Give the extent of all Plasmodium ovale-infected red blood cells.
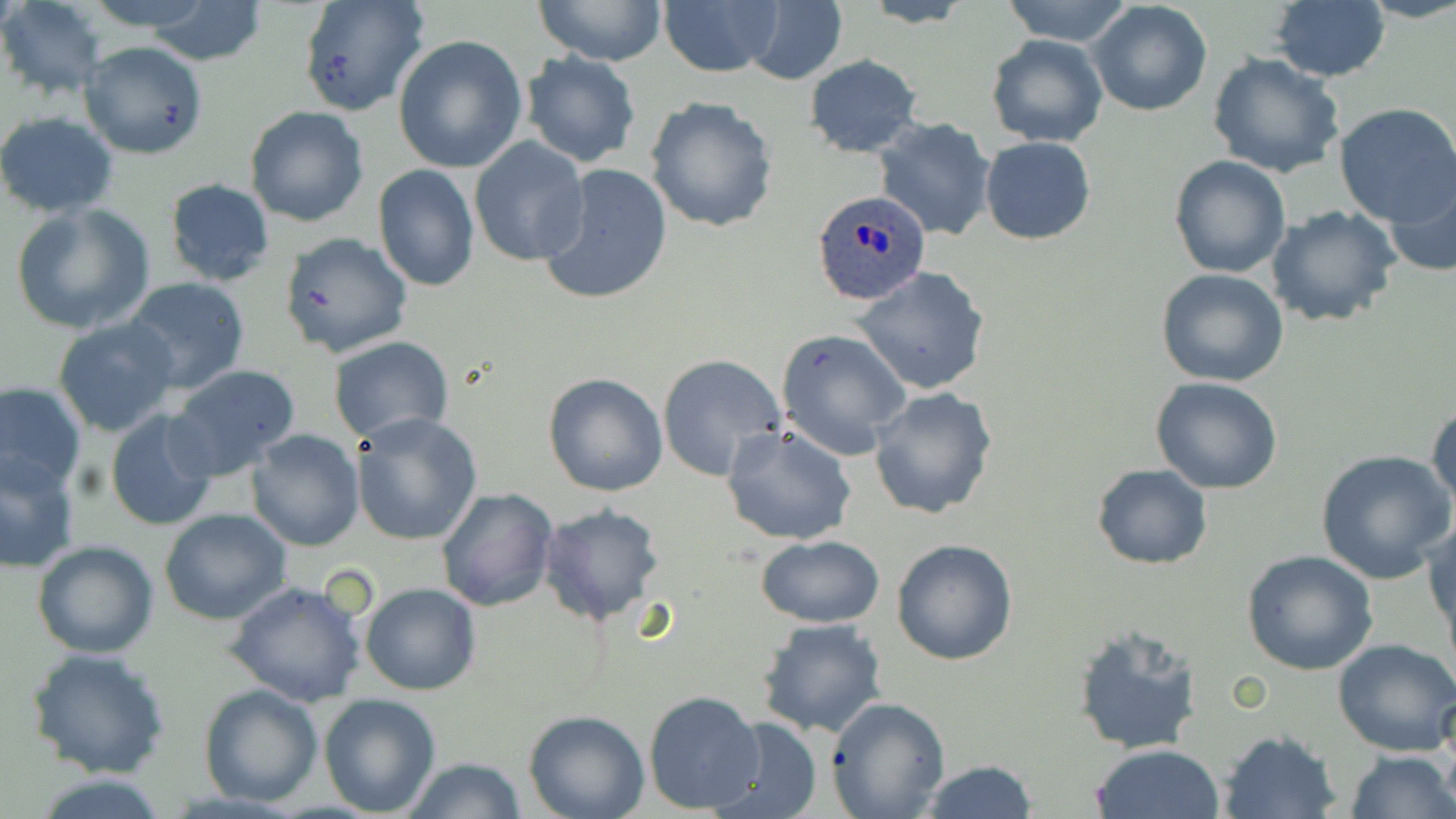

Approximate bounding boxes as (x1, y1, x2, y2) in pixels.
Plasmodium ovale-infected red blood cells: (810, 189, 930, 306).

Uninfected red blood cell locations: (1, 0, 108, 98), (80, 0, 223, 32), (297, 0, 429, 117), (537, 0, 666, 67), (739, 0, 849, 85), (998, 0, 1136, 46), (857, 1, 980, 28), (1268, 1, 1391, 83), (137, 2, 267, 65), (658, 2, 780, 78), (1088, 2, 1213, 118), (392, 34, 528, 173), (985, 34, 1109, 148), (78, 40, 208, 159), (1208, 51, 1344, 178), (521, 52, 640, 168), (804, 54, 922, 158), (646, 95, 779, 232), (1332, 102, 1456, 228), (244, 106, 369, 227), (0, 111, 120, 217), (872, 118, 998, 241), (979, 136, 1096, 244), (470, 137, 591, 267), (1167, 154, 1290, 279), (372, 164, 480, 293), (539, 164, 672, 306), (1385, 169, 1456, 277), (163, 177, 276, 286), (10, 202, 155, 336), (1265, 204, 1401, 327), (280, 234, 415, 357), (854, 266, 991, 395), (1157, 267, 1289, 387), (122, 275, 250, 394), (53, 314, 183, 439), (776, 327, 911, 459), (329, 336, 454, 441), (658, 354, 788, 481), (166, 363, 302, 479), (543, 372, 669, 497), (1152, 378, 1282, 495), (0, 381, 85, 492), (117, 385, 291, 512), (869, 386, 1000, 521), (1427, 400, 1455, 513), (105, 408, 223, 531), (351, 414, 482, 546), (721, 424, 856, 547), (245, 429, 364, 550), (1316, 448, 1453, 584), (0, 451, 81, 574), (1091, 463, 1213, 570), (436, 488, 558, 612), (540, 504, 666, 627), (158, 508, 292, 625), (1425, 515, 1455, 645), (755, 535, 886, 627), (891, 538, 1019, 666), (32, 539, 160, 658), (1240, 550, 1379, 676), (224, 578, 368, 706), (360, 582, 482, 696), (756, 617, 890, 739), (1070, 626, 1203, 757), (1332, 638, 1456, 756), (24, 647, 171, 779), (198, 683, 322, 806), (643, 689, 764, 814), (319, 692, 441, 817), (827, 697, 951, 819), (524, 710, 649, 819), (709, 717, 822, 819), (1218, 729, 1342, 819), (1091, 744, 1226, 819), (1344, 749, 1455, 819), (402, 757, 528, 818), (918, 760, 1039, 818). Slide-level diagnosis: Plasmodium ovale. Thin blood film. Optical microscopy. Image is 1456×819 pixels. Single field of view. Captured at 1000x magnification. May-Grünwald-Giemsa-stained preparation.